Assess the background quality.
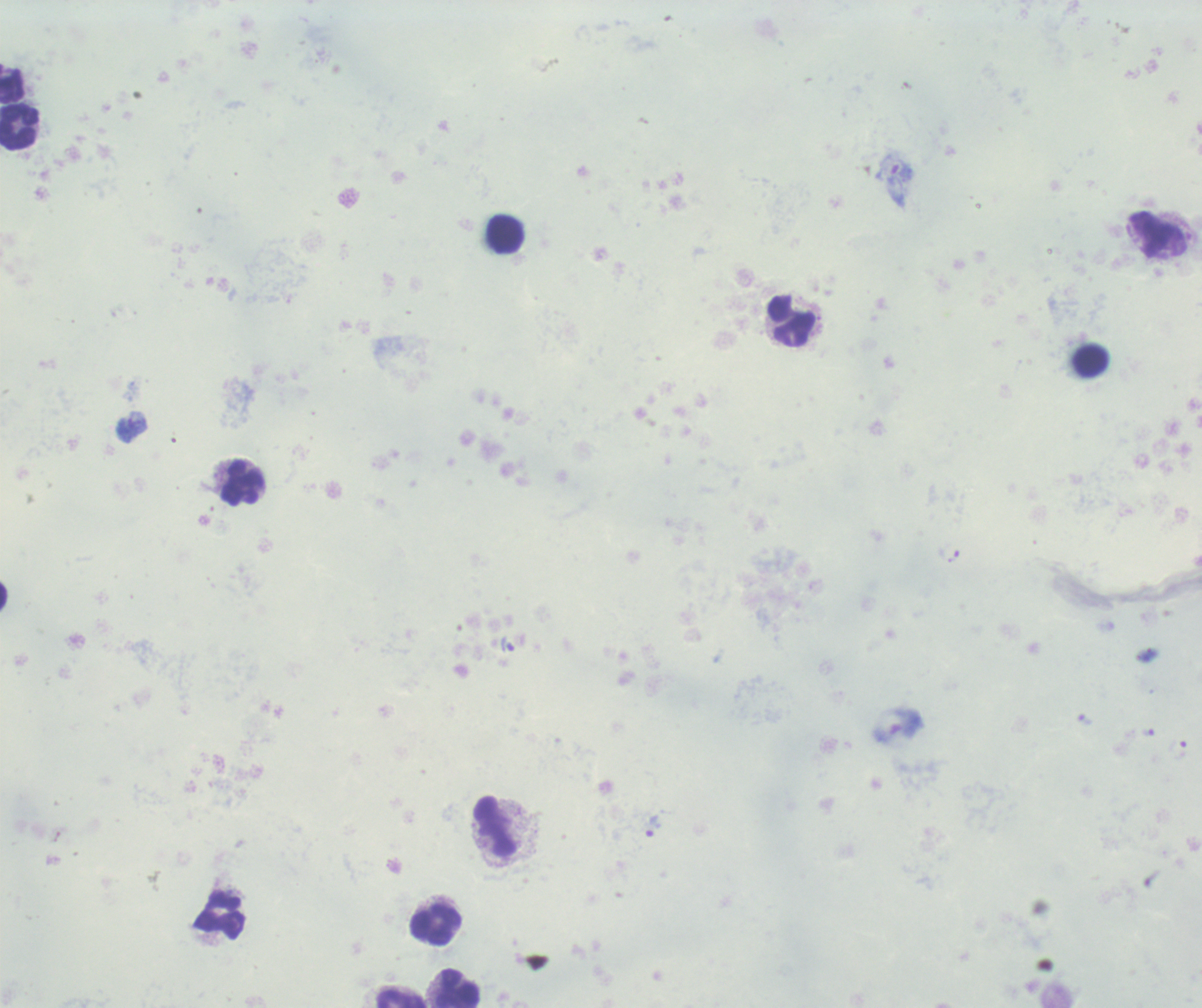

It is poor.

Approximate centers as {x, y} in pixels.
Summary:
  - Trophozoite locations: {507, 644}, {1085, 720}, {1148, 733}, {653, 826}
  - Leukocyte locations: {19, 128}, {505, 234}, {791, 319}, {1090, 361}, {242, 482}, {495, 826}, {220, 917}, {435, 925}, {459, 988}, {401, 998}
  - Stain: Romanowsky
  - Magnification: 100x
  - Context: previously used in a real diagnosis
  - Result: malaria parasites detected
  - Field of view: single
  - Preparation: thick blood film
  - Image size: 1202×1008 pixels